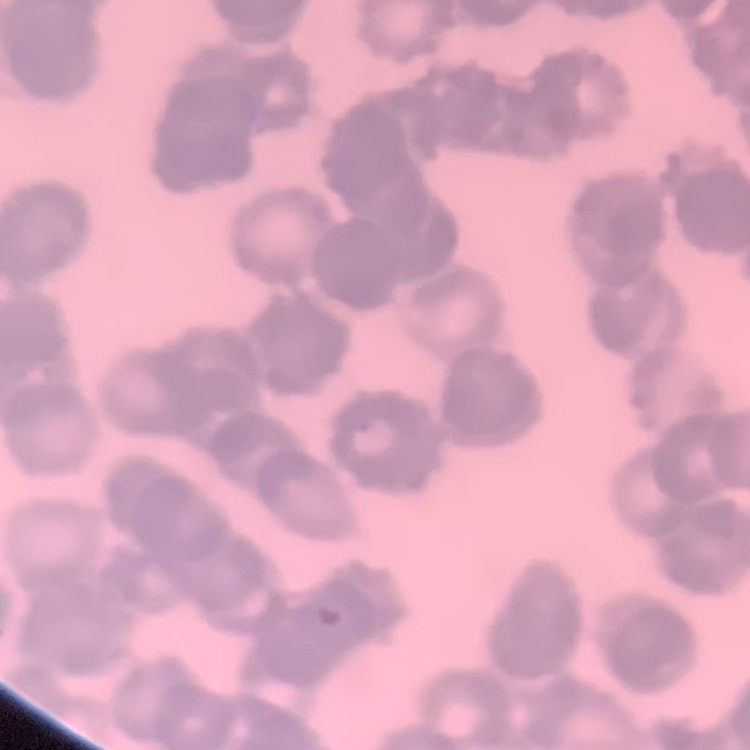
The erythrocytes show rouleaux formation. Square crop of a larger photomicrograph. Stained with either Field's or Giemsa. Thin peripheral smear.